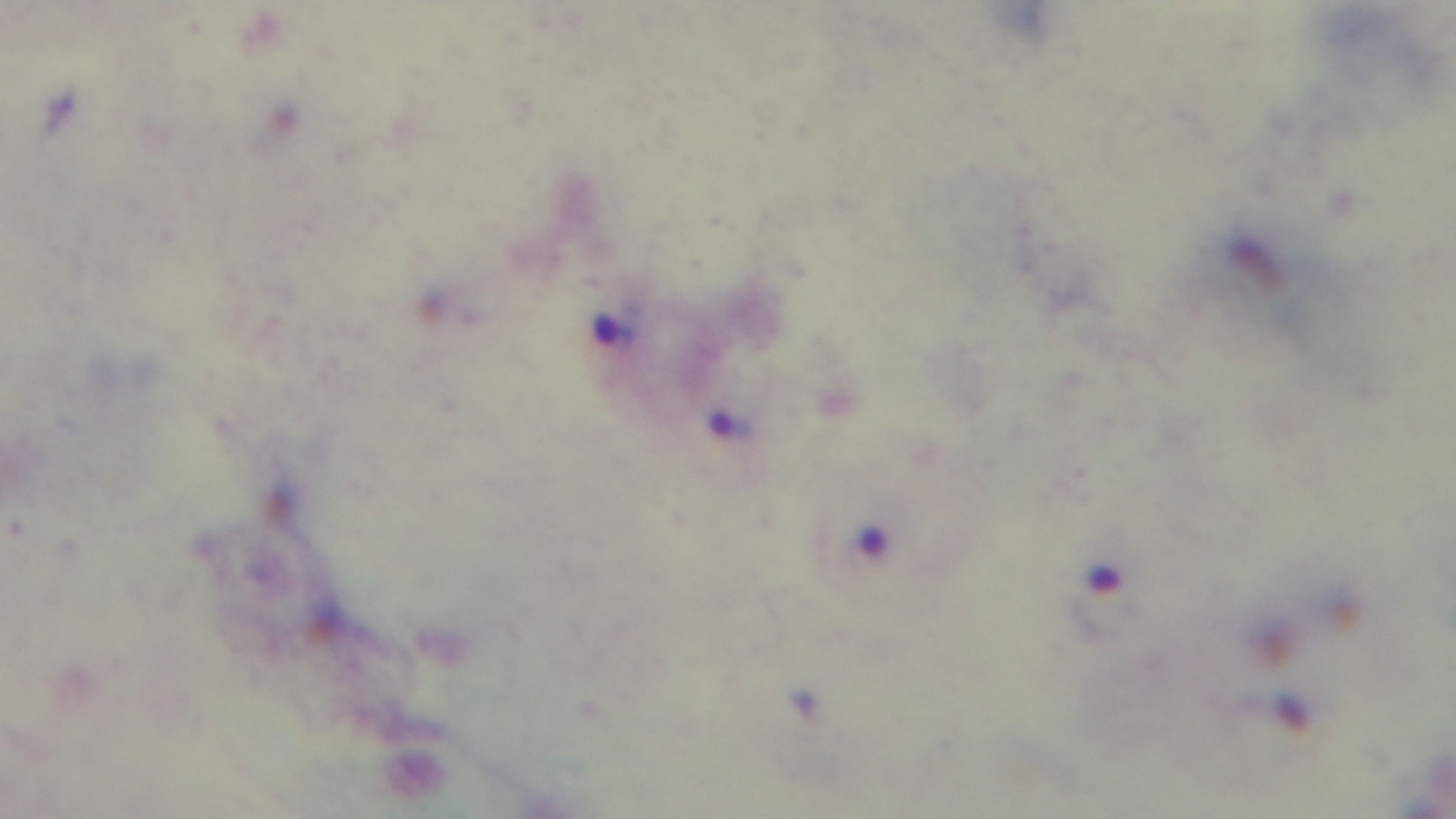
Light microscopy. Giemsa-stained. 100x oil-immersion objective. Preparation: thick smear. Mounted 4K digital camera. Malaria status: positive. Single field of view.